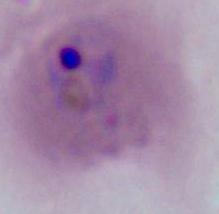
Summary:
  - Identification: Plasmodium
  - Magnification: 400x or 1000x
  - Modality: micrograph